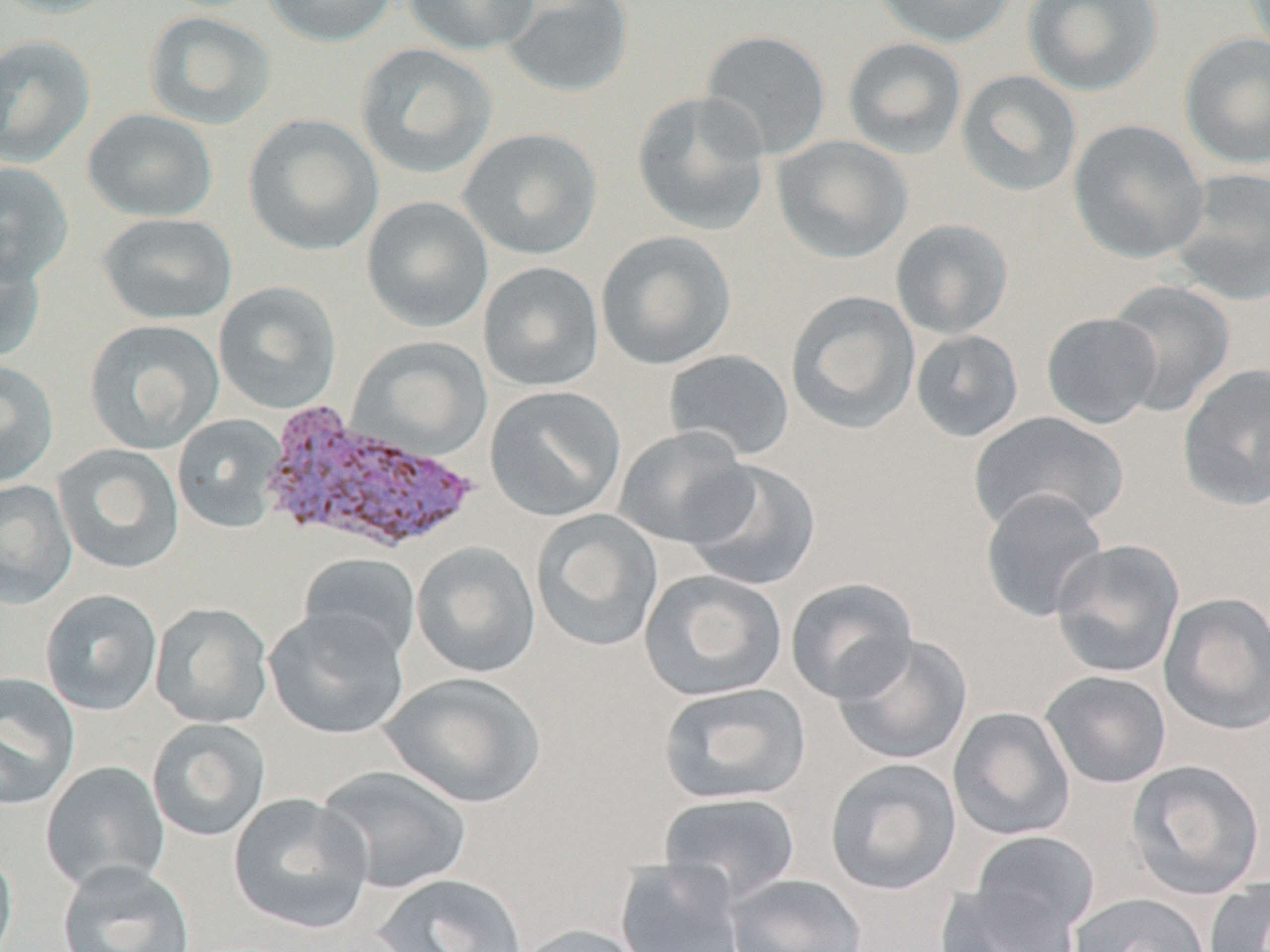
slide_level_diagnosis: Plasmodium vivax
field_of_view: one of a larger specimen
stain: May-Grünwald-Giemsa
uninfected_red_blood_cell_locations: 'approximate bounding boxes as named x1/y1/x2/y2 corners in pixels: (x1=0, y1=0, x2=124, y2=19), (x1=261, y1=0, x2=398, y2=47), (x1=402, y1=0, x2=540, y2=56), (x1=499, y1=0, x2=635, y2=98), (x1=872, y1=0, x2=1017, y2=48), (x1=1022, y1=0, x2=1163, y2=96), (x1=143, y1=12, x2=276, y2=130), (x1=699, y1=29, x2=831, y2=160), (x1=1179, y1=32, x2=1270, y2=171), (x1=0, y1=34, x2=95, y2=168), (x1=842, y1=37, x2=967, y2=159), (x1=354, y1=43, x2=498, y2=180), (x1=955, y1=69, x2=1082, y2=197), (x1=631, y1=90, x2=771, y2=236), (x1=82, y1=107, x2=218, y2=222), (x1=242, y1=114, x2=384, y2=256), (x1=1067, y1=118, x2=1208, y2=263), (x1=457, y1=127, x2=603, y2=260), (x1=771, y1=135, x2=913, y2=264), (x1=0, y1=162, x2=74, y2=286), (x1=1170, y1=167, x2=1270, y2=305), (x1=361, y1=196, x2=494, y2=333), (x1=96, y1=212, x2=238, y2=325), (x1=891, y1=219, x2=1014, y2=339), (x1=595, y1=230, x2=736, y2=370), (x1=0, y1=245, x2=46, y2=364), (x1=478, y1=261, x2=604, y2=392), (x1=1105, y1=280, x2=1236, y2=416), (x1=213, y1=281, x2=342, y2=414), (x1=786, y1=290, x2=920, y2=434), (x1=1041, y1=312, x2=1162, y2=429), (x1=83, y1=318, x2=225, y2=454), (x1=911, y1=329, x2=1024, y2=442), (x1=347, y1=336, x2=493, y2=462), (x1=663, y1=349, x2=795, y2=462), (x1=0, y1=359, x2=59, y2=488), (x1=1177, y1=363, x2=1270, y2=512), (x1=484, y1=385, x2=626, y2=523), (x1=968, y1=411, x2=1128, y2=535), (x1=172, y1=414, x2=286, y2=533), (x1=613, y1=426, x2=756, y2=549), (x1=52, y1=443, x2=185, y2=575), (x1=683, y1=460, x2=822, y2=591), (x1=0, y1=479, x2=78, y2=609), (x1=979, y1=488, x2=1109, y2=623), (x1=530, y1=509, x2=664, y2=652), (x1=1050, y1=539, x2=1185, y2=679), (x1=411, y1=541, x2=541, y2=678), (x1=297, y1=552, x2=422, y2=665), (x1=639, y1=569, x2=788, y2=701), (x1=784, y1=577, x2=919, y2=703), (x1=39, y1=589, x2=163, y2=716), (x1=1158, y1=592, x2=1270, y2=735), (x1=149, y1=602, x2=273, y2=728), (x1=264, y1=608, x2=410, y2=740), (x1=832, y1=632, x2=974, y2=766), (x1=1039, y1=670, x2=1172, y2=789), (x1=0, y1=672, x2=80, y2=811), (x1=379, y1=672, x2=546, y2=808), (x1=657, y1=681, x2=811, y2=806), (x1=948, y1=707, x2=1076, y2=841), (x1=147, y1=718, x2=272, y2=841), (x1=824, y1=757, x2=962, y2=895), (x1=1125, y1=759, x2=1266, y2=900), (x1=40, y1=761, x2=170, y2=892), (x1=316, y1=764, x2=472, y2=894), (x1=658, y1=791, x2=802, y2=902), (x1=227, y1=792, x2=374, y2=935), (x1=968, y1=830, x2=1101, y2=944), (x1=0, y1=844, x2=18, y2=952), (x1=56, y1=859, x2=195, y2=952), (x1=615, y1=859, x2=748, y2=952), (x1=372, y1=872, x2=529, y2=952), (x1=726, y1=873, x2=868, y2=952), (x1=1204, y1=878, x2=1270, y2=952), (x1=936, y1=882, x2=1082, y2=952), (x1=1068, y1=892, x2=1211, y2=952), (x1=511, y1=923, x2=651, y2=952)'
plasmodium_vivax_infected_red_blood_cell_locations: 'approximate bounding boxes as named x1/y1/x2/y2 corners in pixels: (x1=259, y1=398, x2=480, y2=558)'
image_size: 1270×952 pixels
preparation: thin blood smear
magnification: 1000x
modality: light microscopy